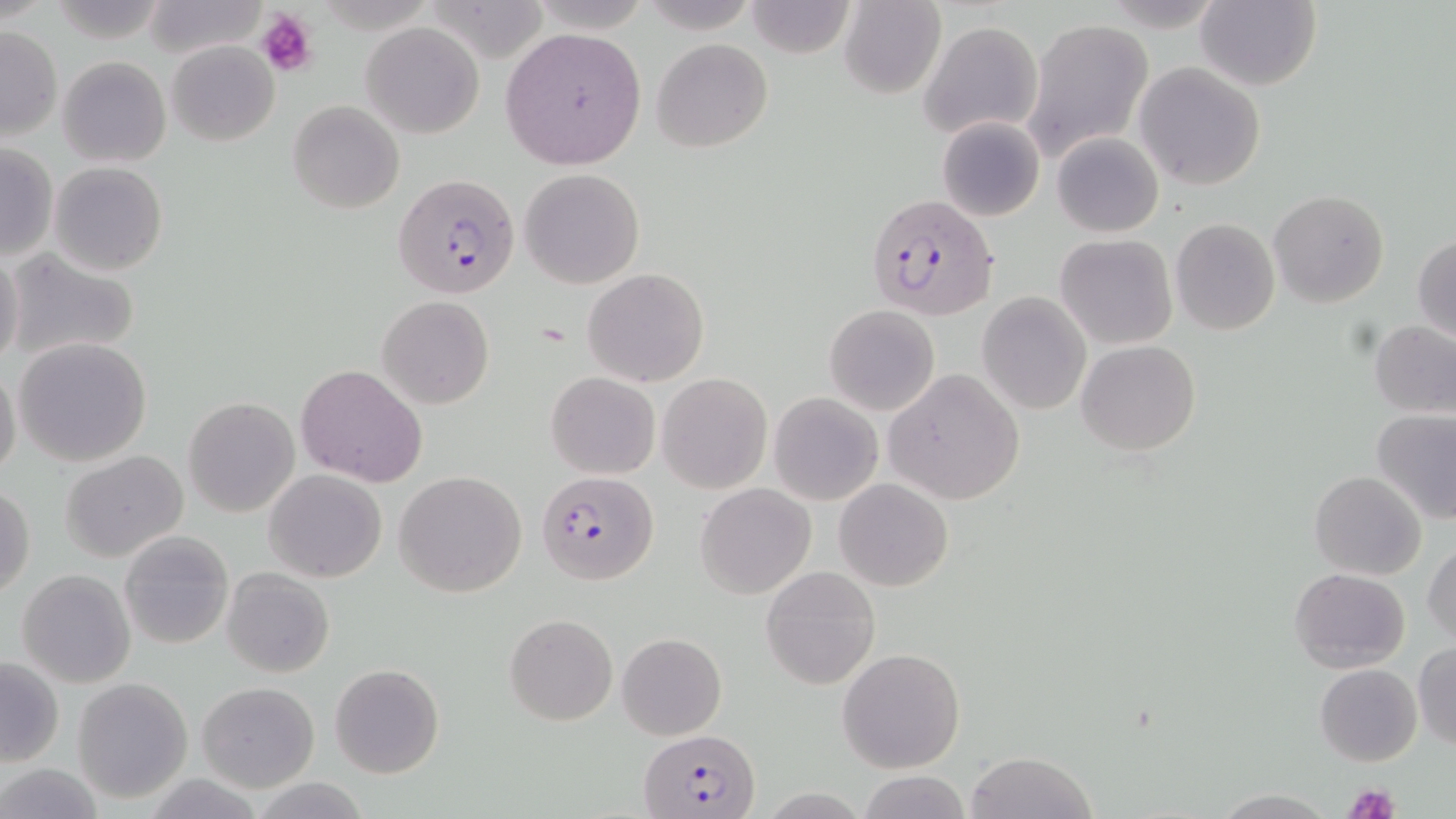
Summary:
  - Coordinate format: approximate bounding boxes as (x1,y1)-(x2,y2) corner pairs in pixels
  - Uninfected red blood cell locations: (141,0)-(267,59), (840,0)-(947,100), (1193,0)-(1321,90), (745,2)-(856,57), (1022,17)-(1152,161), (918,18)-(1046,140), (361,23)-(484,138), (1,26)-(62,140), (500,27)-(647,170), (651,37)-(773,153), (166,39)-(279,148), (58,56)-(171,168), (1135,63)-(1265,191), (288,100)-(405,214), (936,115)-(1046,222), (1053,132)-(1163,237), (0,143)-(57,261), (50,162)-(168,277), (519,168)-(647,289), (1269,189)-(1389,307), (1171,218)-(1279,334), (1412,232)-(1456,344), (1054,234)-(1177,350), (5,249)-(143,365), (0,251)-(24,371), (582,267)-(710,387), (977,292)-(1092,416), (377,296)-(495,408), (825,305)-(940,415), (1370,320)-(1456,417), (13,336)-(152,466), (1076,339)-(1201,455), (0,363)-(22,483), (295,364)-(428,487), (885,368)-(1025,504), (546,372)-(659,479), (658,373)-(771,494), (769,392)-(883,505), (183,397)-(300,518), (1372,411)-(1456,526), (61,451)-(187,563), (264,469)-(385,583), (394,470)-(528,598), (1309,470)-(1427,579), (834,478)-(953,592), (697,483)-(817,599), (1,484)-(35,601), (119,531)-(234,649), (1424,539)-(1456,648), (30,546)-(233,668), (760,566)-(880,689), (1289,567)-(1410,674), (223,568)-(335,678), (17,569)-(137,688), (504,613)-(617,726), (616,632)-(727,740), (1412,640)-(1456,749), (838,647)-(966,772), (0,656)-(64,767), (330,663)-(445,779), (1315,663)-(1422,766), (72,677)-(192,803), (198,682)-(320,793), (965,751)-(1097,819), (0,764)-(105,819), (857,772)-(972,818), (249,777)-(374,818), (1210,789)-(1339,818)
  - Platelet locations: (257,8)-(315,77), (1342,781)-(1400,819)
  - Plasmodium falciparum-infected red blood cell locations: (394,173)-(520,299), (864,195)-(998,321), (537,471)-(658,584), (641,729)-(760,818)
  - Slide-level diagnosis: Plasmodium falciparum
  - Field of view: one of a larger specimen
  - Image size: 1456×819 pixels
  - Preparation: thin blood film
  - Stain: May-Grünwald-Giemsa
  - Magnification: 1000x
  - Modality: light microscopy